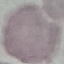

Summary:
  - Malaria status: uninfected
  - Preparation: thin blood smear
  - Capture: smartphone through the microscope eyepiece
  - Image type: automatically extracted cell patch, resized to 64 × 64 pixels
  - Stain: Giemsa